Locate every leukocyte (white blood cell).
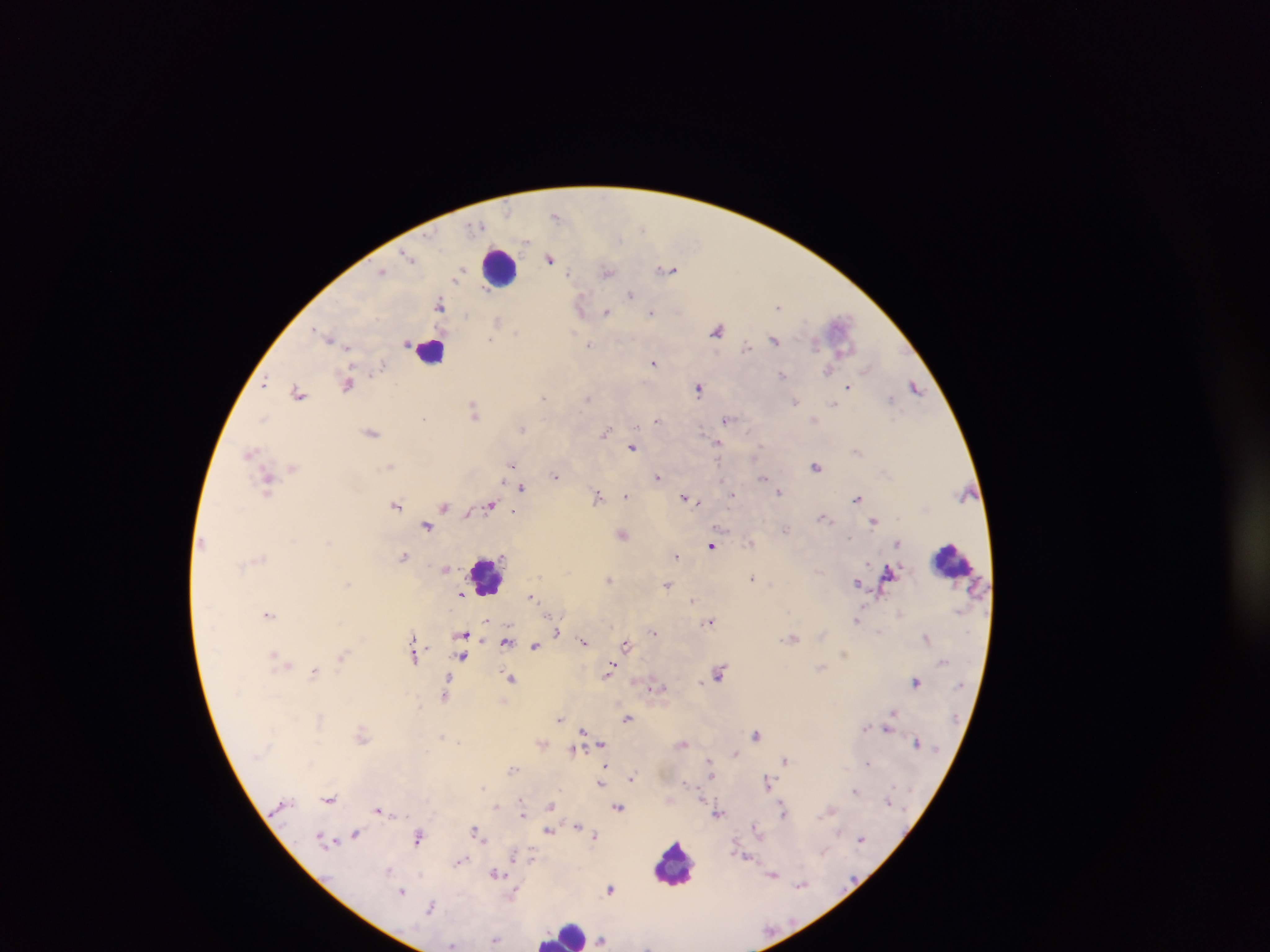

Approximate centers as (x, y) in pixels.
Leukocytes (some below the resolvable threshold): (499, 268), (432, 350), (951, 559), (486, 575), (673, 864), (564, 933).

Plasmodium parasite locations: (556, 216), (477, 226), (642, 228), (407, 255), (549, 258), (668, 269), (382, 270), (607, 272), (459, 273), (569, 273), (631, 295), (440, 304), (581, 305), (779, 306), (607, 312), (651, 312), (497, 320), (717, 330), (516, 333), (329, 337), (774, 339), (491, 340), (815, 343), (407, 344), (589, 344), (746, 346), (347, 347), (654, 363), (382, 365), (866, 369), (827, 371), (783, 373), (265, 381), (348, 384), (916, 386), (849, 387), (698, 388), (298, 392), (543, 398), (587, 398), (890, 399), (795, 402), (834, 404), (475, 410), (264, 418), (423, 418), (657, 420), (728, 420), (814, 420), (522, 428), (372, 432), (605, 432), (718, 443), (632, 448), (758, 451), (250, 452), (754, 455), (390, 465), (511, 465), (817, 466), (293, 468), (556, 476), (657, 476), (763, 478), (722, 480), (268, 483), (523, 488), (779, 492), (626, 495), (733, 495), (598, 496), (686, 498), (857, 498), (396, 505), (490, 505), (445, 506), (514, 511), (825, 518), (874, 520), (426, 526), (786, 529), (622, 535), (850, 538), (750, 543), (897, 544), (711, 545), (676, 555), (403, 556), (446, 569), (753, 578), (609, 579), (348, 583), (858, 583), (668, 584), (461, 594), (532, 597), (692, 600), (268, 615), (856, 620), (487, 621), (710, 621), (557, 632), (654, 632), (464, 635), (793, 638), (926, 638), (507, 641), (583, 641), (626, 644), (535, 646), (843, 653), (415, 655), (274, 656), (342, 656), (462, 656), (280, 659), (286, 663), (611, 668), (821, 668), (315, 672), (720, 673), (511, 679), (916, 682), (656, 686), (445, 692), (892, 712), (560, 718), (627, 718), (865, 727), (887, 729), (584, 731), (756, 734), (362, 736), (442, 737), (458, 742), (601, 743), (683, 743), (917, 743), (573, 750), (736, 753), (710, 760), (785, 760), (867, 763), (605, 766), (513, 770), (711, 775), (632, 778), (686, 782), (600, 783), (768, 783), (483, 787), (855, 791), (330, 799), (523, 803), (551, 805), (496, 806), (618, 807), (379, 810), (830, 810), (783, 811), (522, 812), (719, 814), (577, 826), (755, 826), (476, 831), (549, 831), (839, 832), (356, 834), (594, 836), (418, 837), (861, 839), (325, 841), (824, 850), (515, 855), (531, 857), (461, 861), (389, 871), (495, 873), (773, 874), (801, 885), (610, 889), (403, 891), (515, 892), (430, 908), (496, 939), (602, 939), (452, 946). Image is 1270×952 pixels. Single field of view. Sample from Ghana. Thick blood film. Photographed through a microscope with a mobile-phone camera.